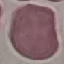 Result: no malaria parasites seen. Thin blood smear. Automatically extracted cell patch, resized to 64 × 64 pixels. Photographed with a smartphone camera at the microscope eyepiece. Giemsa stain.